Outline each blood parasite and name the species.
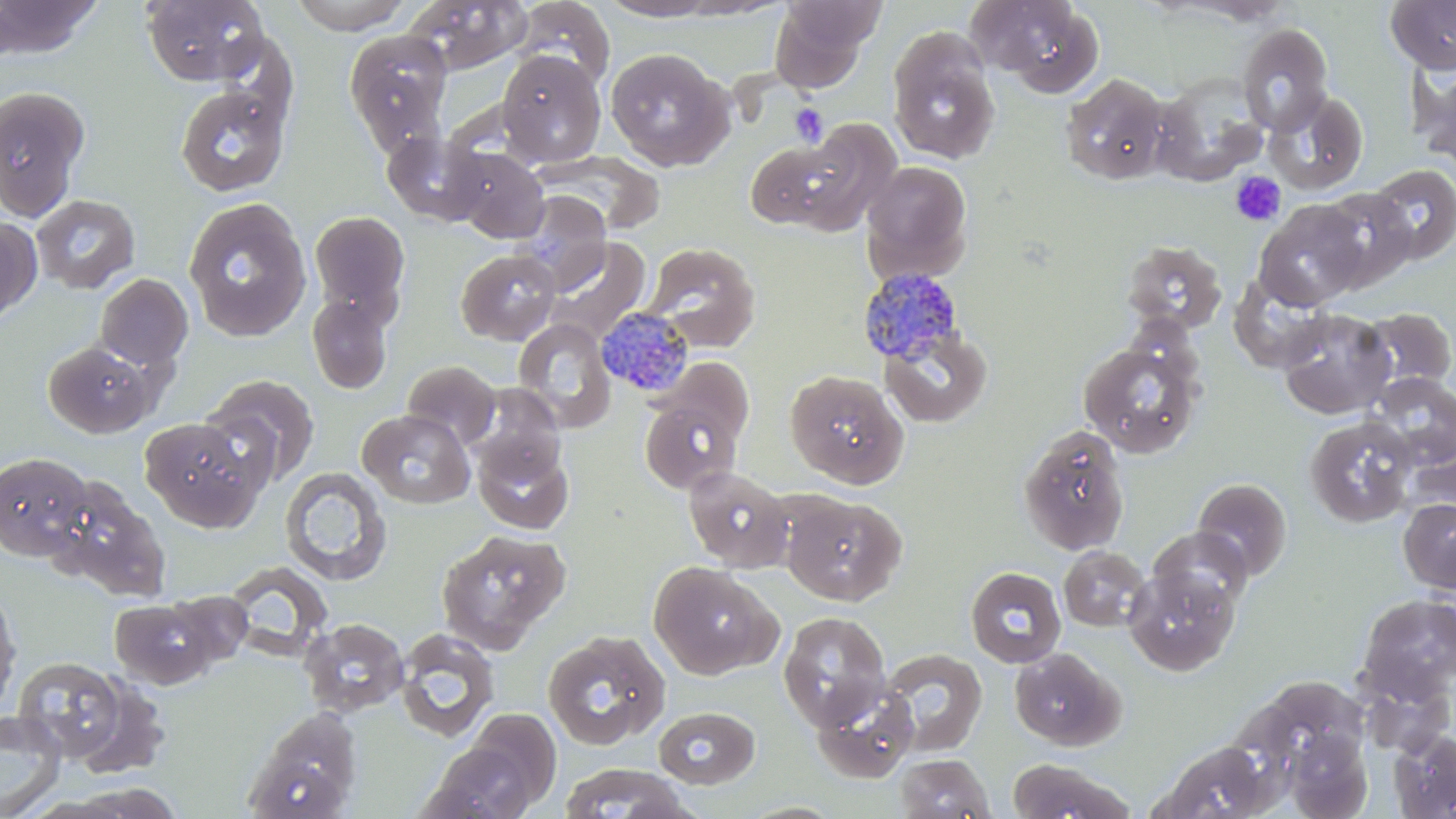

Approximate bounding boxes as (x1, y1, x2, y2) in pixels.
Plasmodium malariae-infected red blood cells: (858, 268, 965, 366), (596, 307, 695, 399).
No Plasmodium falciparum, Plasmodium ovale, Plasmodium vivax, Babesia divergens, or Trypanosoma brucei observed.

slide-level diagnosis = Plasmodium malariae
magnification = 1000x
image size = 1456×819 pixels
stain = May-Grünwald-Giemsa
modality = light microscopy
uninfected red blood cell locations = approximate bounding boxes as (x1, y1, x2, y2) in pixels: (0, 0, 103, 60), (140, 0, 269, 86), (288, 0, 413, 34), (402, 0, 532, 75), (513, 0, 614, 88), (599, 0, 721, 21), (969, 0, 1106, 96), (1385, 0, 1456, 75), (769, 1, 880, 91), (1236, 22, 1333, 134), (887, 28, 1000, 165), (344, 30, 454, 155), (604, 48, 732, 171), (496, 49, 606, 167), (1414, 63, 1456, 174), (1060, 72, 1171, 185), (1152, 73, 1268, 187), (173, 83, 292, 197), (0, 86, 91, 221), (1267, 90, 1369, 193), (787, 118, 904, 237), (383, 132, 488, 226), (744, 138, 857, 230), (453, 149, 549, 243), (536, 153, 665, 235), (860, 160, 973, 281), (1369, 164, 1456, 263), (1316, 188, 1418, 291), (515, 191, 611, 291), (30, 194, 140, 294), (183, 197, 311, 342), (1253, 200, 1367, 310), (309, 211, 410, 321), (0, 215, 42, 326), (545, 237, 651, 344), (1121, 239, 1228, 336), (644, 242, 761, 351), (455, 249, 560, 345), (94, 273, 193, 372), (1230, 274, 1335, 373), (307, 291, 393, 394), (1277, 307, 1396, 419), (1360, 308, 1455, 394), (513, 318, 616, 433), (879, 327, 993, 428), (42, 340, 159, 438), (1078, 342, 1202, 459), (402, 360, 500, 449), (785, 370, 908, 488), (1369, 373, 1456, 468), (203, 374, 321, 485), (638, 393, 746, 493), (358, 409, 475, 508), (1304, 416, 1417, 528), (140, 417, 269, 532), (1018, 426, 1130, 556), (1403, 429, 1456, 519), (473, 437, 575, 535), (0, 450, 94, 560), (683, 465, 794, 572), (280, 467, 392, 586), (46, 476, 171, 601), (1192, 477, 1293, 582), (781, 493, 906, 606), (1397, 498, 1456, 594), (1148, 527, 1253, 614), (435, 529, 571, 652), (1059, 546, 1150, 631), (649, 562, 777, 680), (1123, 565, 1240, 676), (965, 566, 1066, 668), (0, 590, 21, 714), (1356, 593, 1456, 702), (109, 598, 218, 688), (777, 612, 892, 731), (300, 618, 409, 717), (394, 629, 499, 743), (544, 629, 671, 749), (878, 648, 988, 757), (1009, 648, 1125, 750), (12, 657, 129, 762), (68, 674, 172, 780), (810, 679, 919, 784), (653, 706, 761, 789), (459, 707, 562, 811), (243, 709, 364, 819), (0, 710, 67, 818), (1282, 727, 1372, 817), (1389, 729, 1456, 819), (421, 740, 539, 819), (1154, 741, 1278, 818), (894, 753, 995, 819), (1008, 759, 1136, 819), (558, 764, 694, 818), (46, 783, 190, 819)
preparation = thin blood smear
field of view = single
platelet locations = approximate bounding boxes as (x1, y1, x2, y2) in pixels: (790, 104, 827, 147), (1230, 171, 1286, 226)